Name the parasite shown.
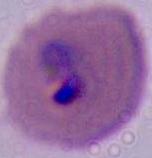
Plasmodium.

Micrograph. Captured at either 400x or 1000x magnification.